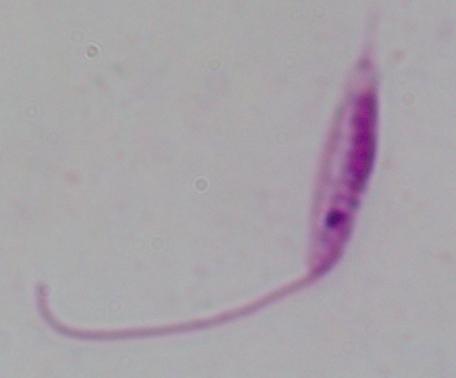
{
  "identification": "Leishmania",
  "magnification": "1000x",
  "modality": "micrograph"
}